State which parasite is depicted.
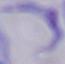

This is a trypanosome.

Captured at 1000x magnification. Photomicrograph.